Outline each Plasmodium vivax-infected red blood cell.
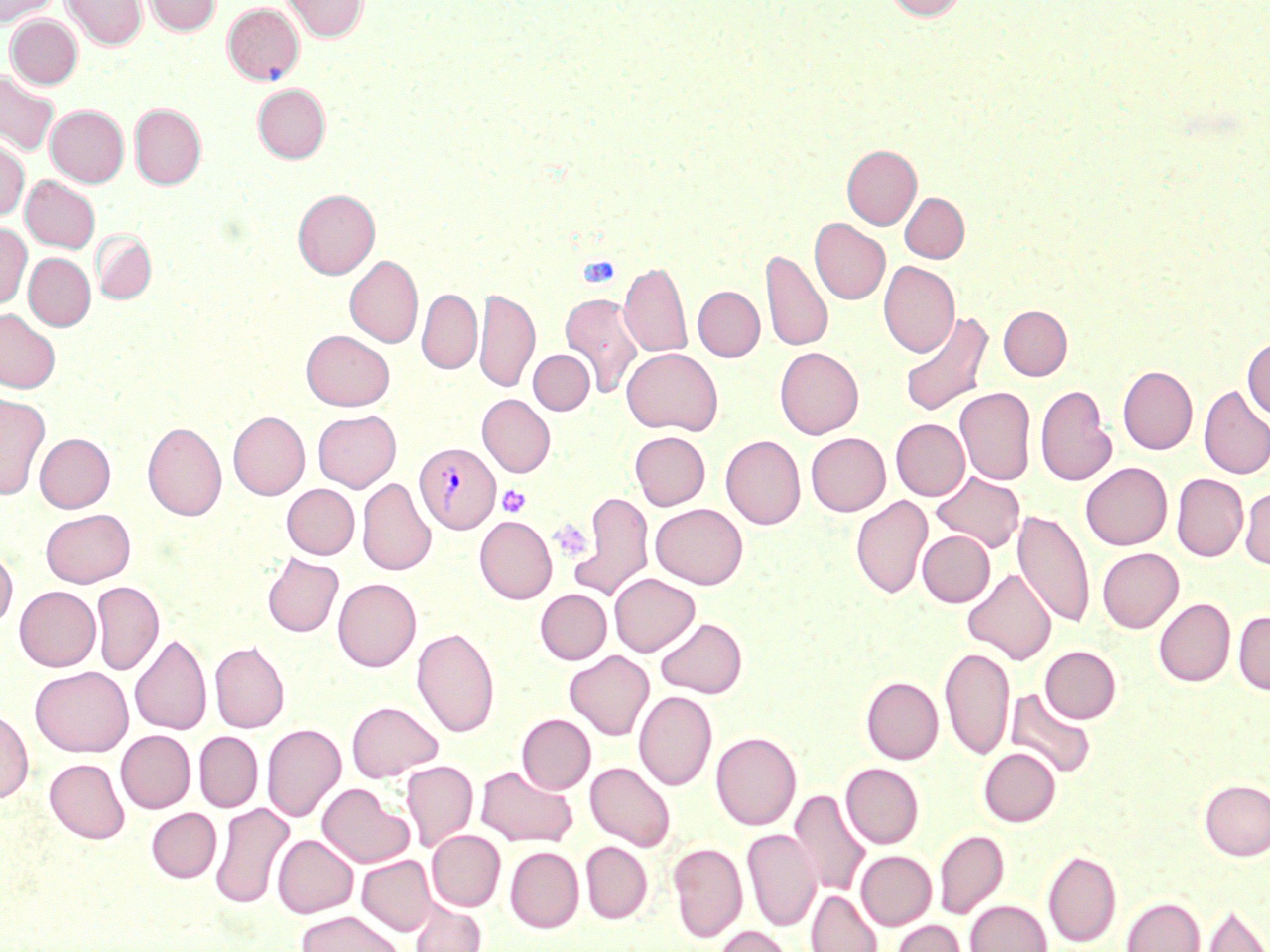
Approximate bounding boxes as (x1, y1, x2, y2) in pixels.
Plasmodium vivax-infected red blood cells: (415, 443, 500, 534).

Uninfected red blood cell locations: (0, 0, 58, 26), (61, 0, 148, 50), (143, 0, 221, 35), (282, 0, 369, 42), (884, 0, 969, 21), (222, 2, 304, 85), (6, 15, 82, 89), (0, 70, 60, 156), (253, 84, 330, 163), (130, 103, 206, 190), (46, 105, 128, 187), (0, 139, 29, 220), (842, 144, 921, 229), (21, 175, 100, 253), (293, 189, 379, 279), (900, 192, 969, 263), (810, 218, 889, 304), (0, 223, 31, 309), (92, 231, 157, 304), (761, 249, 832, 353), (24, 253, 95, 330), (345, 255, 423, 348), (619, 261, 692, 358), (878, 261, 960, 357), (693, 286, 764, 361), (417, 288, 481, 374), (475, 288, 540, 392), (560, 292, 644, 398), (998, 306, 1072, 380), (0, 309, 60, 393), (899, 311, 994, 418), (301, 330, 394, 410), (1242, 336, 1270, 420), (775, 347, 864, 439), (621, 348, 723, 435), (528, 350, 593, 414), (1118, 366, 1197, 454), (1035, 384, 1117, 487), (1198, 385, 1270, 479), (955, 387, 1036, 486), (0, 392, 50, 499), (477, 394, 555, 477), (312, 410, 401, 492), (228, 411, 310, 500), (891, 419, 970, 500), (143, 422, 226, 520), (630, 431, 710, 510), (805, 432, 890, 516), (34, 433, 115, 512), (721, 435, 805, 529), (1081, 462, 1172, 549), (932, 471, 1024, 552), (1171, 474, 1248, 561), (357, 477, 436, 575), (282, 484, 359, 559), (1239, 486, 1270, 569), (571, 491, 654, 602), (850, 495, 933, 599), (650, 503, 748, 589), (41, 508, 135, 587), (1013, 509, 1094, 629), (475, 516, 557, 604), (918, 530, 995, 607), (0, 547, 17, 628), (1097, 548, 1183, 633), (262, 553, 343, 637), (962, 568, 1056, 664), (609, 573, 700, 656), (333, 578, 421, 671), (90, 581, 164, 675), (14, 586, 100, 671), (536, 589, 612, 664), (1154, 598, 1235, 686), (1233, 610, 1270, 695), (655, 617, 747, 698), (412, 627, 500, 738), (130, 633, 211, 736), (210, 640, 290, 733), (940, 646, 1014, 761), (1040, 646, 1121, 723), (564, 650, 654, 740), (30, 666, 133, 756), (861, 676, 943, 764), (1006, 688, 1096, 779), (634, 690, 717, 790), (346, 700, 443, 781), (0, 708, 33, 804), (517, 714, 595, 794), (262, 724, 346, 822), (116, 730, 195, 812), (194, 731, 263, 812), (711, 731, 801, 830), (979, 748, 1060, 826), (45, 759, 129, 843), (401, 761, 478, 851), (585, 762, 676, 851), (841, 763, 924, 848), (475, 765, 578, 846), (1199, 779, 1270, 860), (317, 783, 414, 868), (789, 789, 870, 897), (210, 802, 295, 909), (147, 808, 221, 882), (742, 829, 820, 931), (426, 830, 505, 911), (935, 830, 1008, 919), (273, 835, 358, 918), (580, 842, 653, 923), (668, 842, 747, 942), (505, 847, 584, 933), (1043, 849, 1121, 947), (856, 851, 937, 930), (357, 855, 437, 935), (806, 890, 882, 952), (1121, 896, 1205, 952), (965, 900, 1052, 952), (411, 901, 486, 952), (1201, 902, 1270, 952), (297, 910, 404, 952), (889, 919, 967, 952), (715, 925, 794, 952). Platelet locations: (497, 484, 531, 518), (549, 517, 592, 562). Slide-level diagnosis: Plasmodium vivax. Image is 1270×952 pixels. May-Grünwald-Giemsa stain. Light microscopy. Thin blood film. 1000x magnification. One field of a larger specimen.